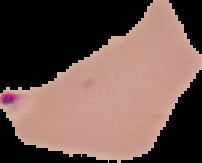

{
  "preparation": "thin blood smear",
  "image_type": "segmented cell region with the area outside set to black",
  "malaria_status": "parasitized",
  "image_size": "202×163 pixels"
}